Comment on the morphology of the erythrocytes.
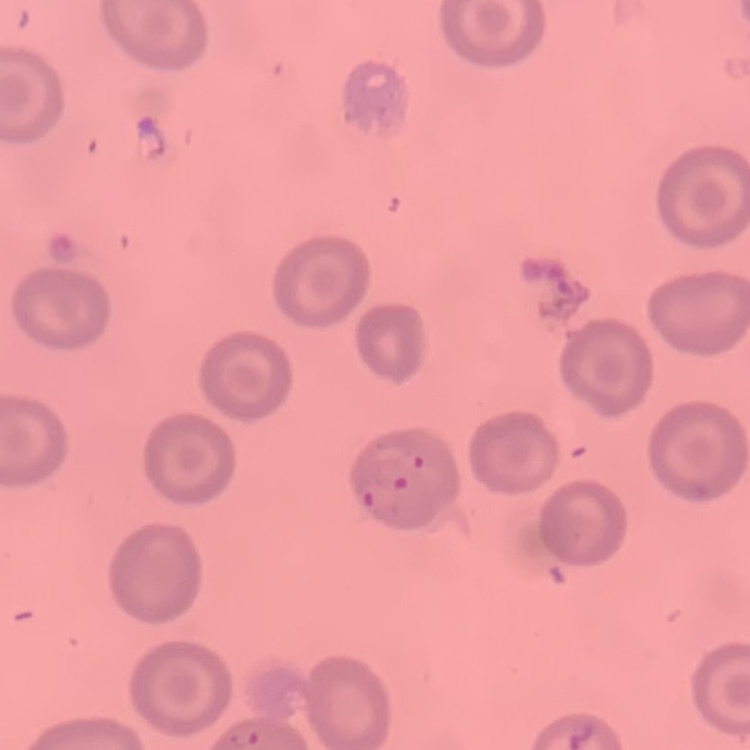
No rouleaux formation.

Summary:
  - Image type: square crop of a larger photomicrograph
  - Stain: Field's or Giemsa
  - Preparation: thin peripheral smear